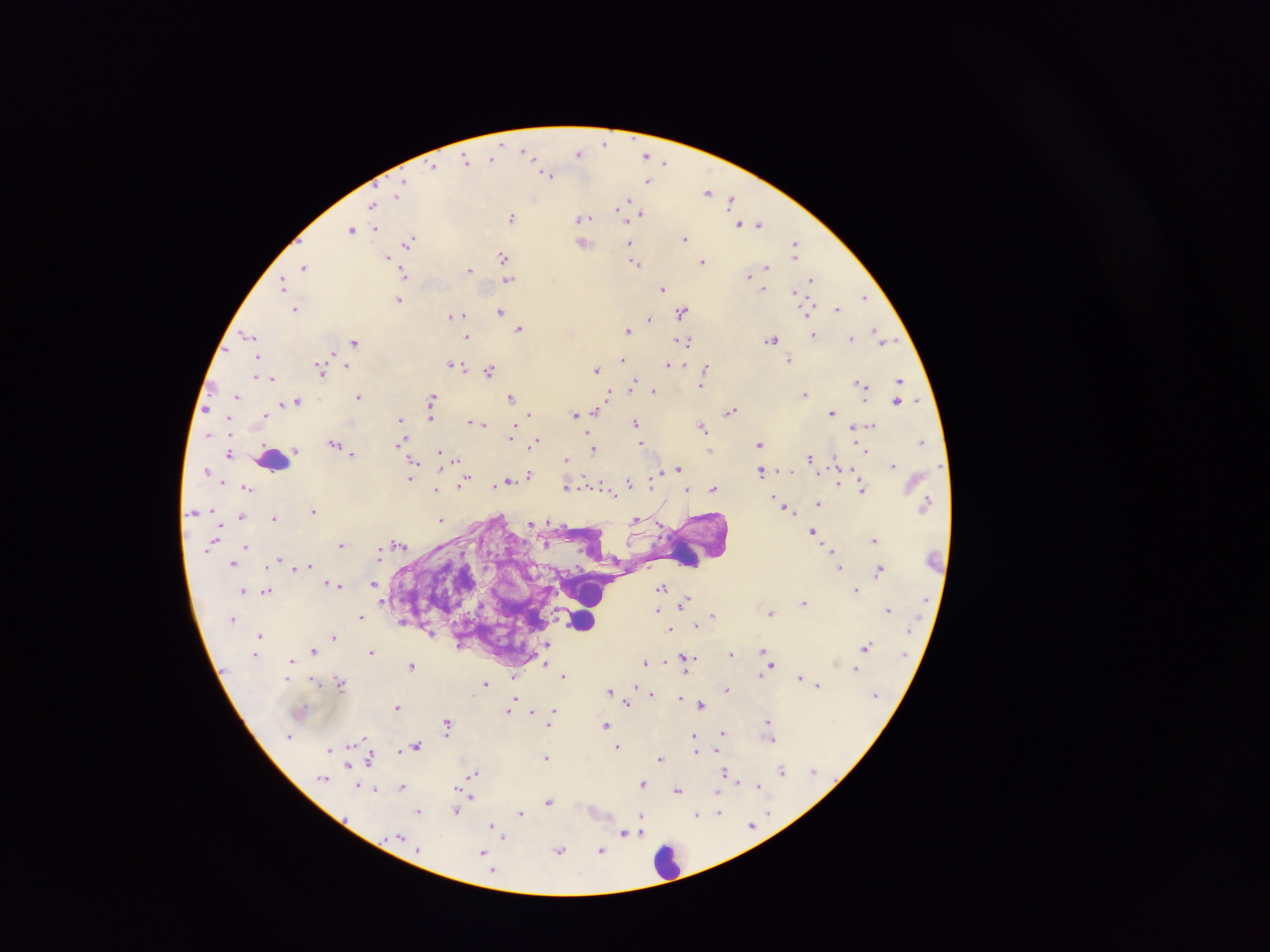
Approximate centers as {x, y} in pixels. Malaria parasite locations: {605, 142}, {526, 152}, {578, 153}, {646, 155}, {466, 159}, {491, 159}, {665, 161}, {433, 166}, {548, 174}, {649, 180}, {708, 191}, {399, 192}, {732, 200}, {626, 201}, {373, 205}, {621, 206}, {618, 209}, {641, 214}, {512, 217}, {582, 218}, {740, 223}, {750, 223}, {760, 224}, {375, 228}, {351, 229}, {684, 239}, {410, 240}, {583, 243}, {630, 245}, {795, 246}, {503, 255}, {387, 256}, {702, 262}, {636, 263}, {305, 267}, {767, 267}, {469, 269}, {405, 275}, {748, 275}, {507, 280}, {810, 280}, {283, 285}, {663, 288}, {764, 288}, {795, 293}, {865, 296}, {399, 300}, {295, 309}, {838, 309}, {500, 311}, {682, 312}, {808, 312}, {453, 315}, {649, 319}, {520, 329}, {628, 330}, {813, 334}, {877, 334}, {249, 335}, {467, 336}, {852, 338}, {772, 339}, {884, 340}, {684, 341}, {355, 342}, {257, 358}, {623, 360}, {789, 360}, {452, 364}, {669, 364}, {347, 365}, {706, 368}, {319, 369}, {596, 369}, {489, 370}, {256, 375}, {705, 375}, {272, 378}, {899, 380}, {860, 383}, {633, 384}, {702, 384}, {653, 390}, {610, 393}, {805, 393}, {237, 395}, {359, 396}, {511, 397}, {431, 398}, {898, 400}, {298, 402}, {284, 404}, {206, 408}, {596, 410}, {730, 412}, {832, 412}, {530, 414}, {574, 414}, {265, 416}, {430, 417}, {400, 421}, {471, 421}, {636, 422}, {482, 424}, {870, 425}, {702, 427}, {854, 428}, {512, 434}, {535, 441}, {921, 441}, {402, 442}, {641, 443}, {333, 444}, {759, 444}, {344, 449}, {594, 449}, {295, 451}, {865, 451}, {229, 453}, {353, 454}, {440, 454}, {810, 457}, {566, 459}, {413, 460}, {892, 464}, {412, 469}, {678, 469}, {761, 472}, {529, 474}, {410, 477}, {655, 477}, {508, 481}, {464, 482}, {629, 482}, {838, 482}, {567, 485}, {713, 488}, {247, 489}, {687, 489}, {863, 489}, {436, 490}, {610, 490}, {818, 503}, {785, 508}, {313, 510}, {241, 517}, {274, 517}, {442, 518}, {636, 519}, {548, 520}, {530, 523}, {813, 532}, {875, 539}, {399, 544}, {341, 545}, {245, 546}, {831, 550}, {379, 553}, {279, 559}, {233, 563}, {309, 565}, {839, 567}, {295, 568}, {880, 570}, {374, 584}, {339, 585}, {662, 588}, {243, 590}, {856, 590}, {267, 591}, {686, 600}, {804, 602}, {657, 609}, {888, 610}, {713, 613}, {771, 613}, {360, 616}, {697, 625}, {670, 629}, {260, 635}, {334, 636}, {546, 647}, {865, 647}, {763, 649}, {313, 650}, {371, 652}, {730, 653}, {256, 654}, {688, 657}, {694, 657}, {290, 661}, {645, 662}, {664, 663}, {545, 664}, {687, 664}, {411, 665}, {771, 665}, {855, 669}, {564, 675}, {761, 676}, {800, 676}, {513, 678}, {340, 682}, {485, 684}, {818, 685}, {610, 690}, {727, 690}, {651, 693}, {680, 699}, {628, 703}, {701, 704}, {397, 707}, {510, 707}, {553, 711}, {532, 712}, {768, 722}, {446, 724}, {605, 725}, {723, 732}, {289, 736}, {694, 737}, {772, 740}, {416, 746}, {618, 747}, {330, 749}, {696, 749}, {718, 750}, {546, 757}, {370, 758}, {660, 759}, {348, 765}, {813, 770}, {782, 771}, {474, 773}, {725, 773}, {322, 778}, {737, 782}, {642, 784}, {403, 786}, {758, 787}, {374, 790}, {678, 790}, {718, 790}, {471, 798}, {549, 801}, {419, 811}, {456, 811}, {719, 812}, {521, 813}, {769, 813}, {697, 815}, {642, 822}, {752, 825}, {494, 828}, {638, 829}, {624, 833}, {401, 838}, {559, 851}, {600, 851}, {484, 853}. Leukocyte locations: {273, 461}, {687, 554}, {592, 593}, {582, 620}, {668, 861}. Photographed through a microscope with a mobile-phone camera. One field of view. Thick blood film. Collected in Ghana. Image is 1270×952 pixels.